Name the blood parasite species.
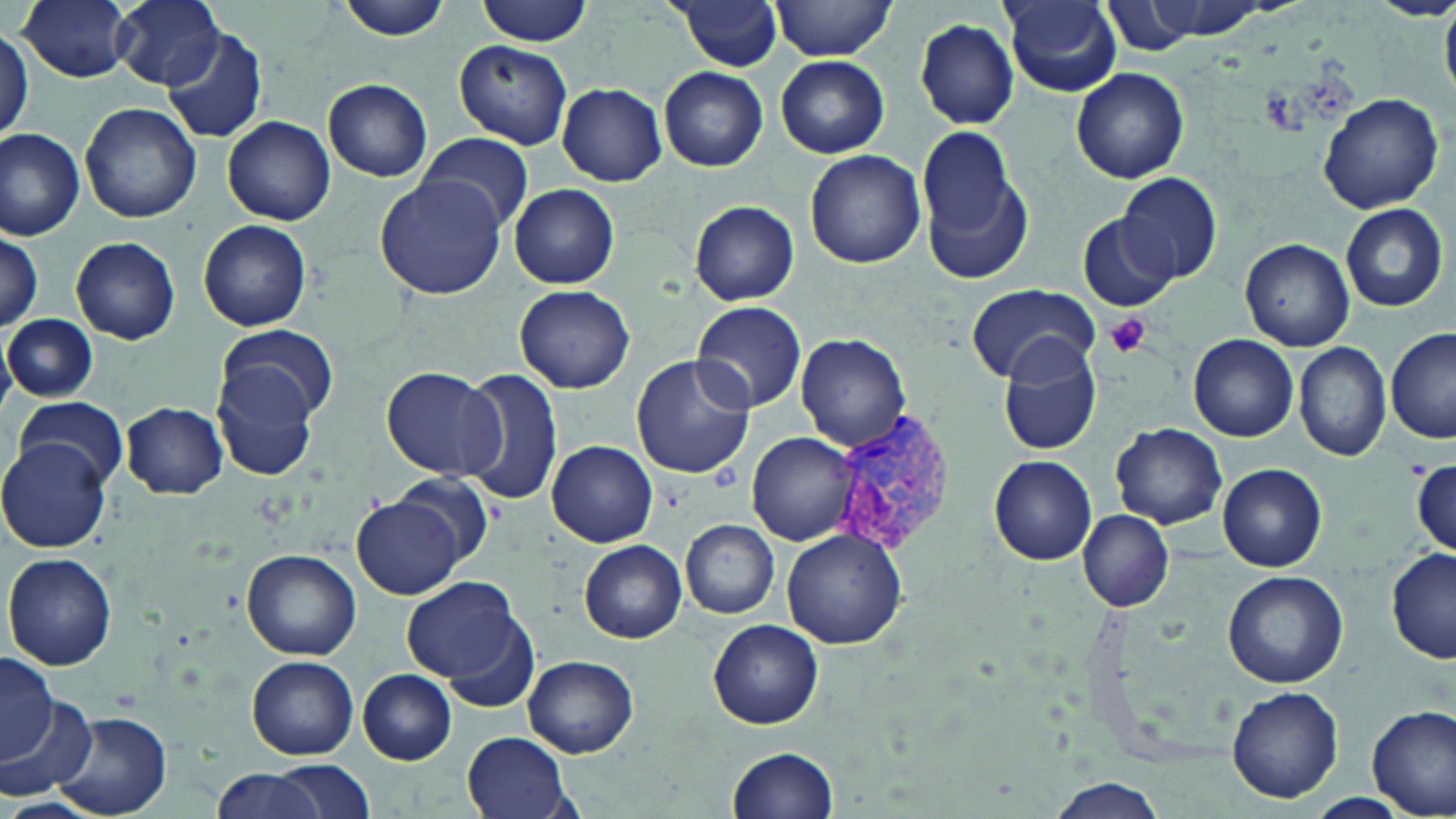

Plasmodium vivax.

Summary:
  - Coordinate format: approximate bounding boxes as named x1/y1/x2/y2 corners in pixels
  - Plasmodium vivax-infected red blood cell locations: (x1=822, y1=416, x2=953, y2=559)
  - Uninfected red blood cell locations: (x1=17, y1=0, x2=134, y2=83), (x1=114, y1=0, x2=225, y2=90), (x1=333, y1=0, x2=454, y2=41), (x1=477, y1=0, x2=593, y2=45), (x1=673, y1=0, x2=783, y2=72), (x1=768, y1=0, x2=902, y2=61), (x1=1100, y1=0, x2=1203, y2=55), (x1=1371, y1=0, x2=1456, y2=21), (x1=1001, y1=1, x2=1123, y2=97), (x1=915, y1=18, x2=1020, y2=129), (x1=0, y1=29, x2=32, y2=143), (x1=162, y1=29, x2=267, y2=142), (x1=453, y1=41, x2=573, y2=150), (x1=777, y1=56, x2=889, y2=158), (x1=1070, y1=66, x2=1189, y2=184), (x1=659, y1=67, x2=767, y2=172), (x1=323, y1=78, x2=433, y2=182), (x1=557, y1=83, x2=667, y2=185), (x1=1318, y1=93, x2=1443, y2=213), (x1=80, y1=102, x2=202, y2=222), (x1=222, y1=114, x2=335, y2=225), (x1=917, y1=125, x2=1028, y2=272), (x1=0, y1=126, x2=87, y2=239), (x1=417, y1=132, x2=534, y2=233), (x1=804, y1=149, x2=924, y2=269), (x1=1115, y1=171, x2=1224, y2=284), (x1=374, y1=176, x2=508, y2=299), (x1=509, y1=184, x2=620, y2=289), (x1=689, y1=201, x2=799, y2=305), (x1=1339, y1=203, x2=1448, y2=313), (x1=1077, y1=212, x2=1179, y2=310), (x1=198, y1=218, x2=311, y2=331), (x1=0, y1=230, x2=43, y2=334), (x1=69, y1=235, x2=181, y2=345), (x1=1240, y1=239, x2=1355, y2=350), (x1=514, y1=284, x2=634, y2=393), (x1=964, y1=284, x2=1099, y2=384), (x1=691, y1=300, x2=808, y2=414), (x1=3, y1=313, x2=96, y2=403), (x1=220, y1=326, x2=339, y2=426), (x1=1386, y1=327, x2=1456, y2=442), (x1=793, y1=332, x2=912, y2=451), (x1=1189, y1=334, x2=1299, y2=440), (x1=1294, y1=342, x2=1391, y2=462), (x1=996, y1=344, x2=1100, y2=456), (x1=630, y1=356, x2=756, y2=479), (x1=214, y1=366, x2=322, y2=483), (x1=382, y1=367, x2=505, y2=480), (x1=457, y1=368, x2=564, y2=508), (x1=15, y1=395, x2=132, y2=492), (x1=120, y1=402, x2=228, y2=498), (x1=1110, y1=422, x2=1228, y2=529), (x1=748, y1=432, x2=864, y2=545), (x1=0, y1=437, x2=112, y2=552), (x1=546, y1=440, x2=658, y2=547), (x1=989, y1=456, x2=1096, y2=565), (x1=1413, y1=458, x2=1454, y2=557), (x1=1217, y1=463, x2=1327, y2=571), (x1=394, y1=473, x2=494, y2=565), (x1=354, y1=496, x2=463, y2=598), (x1=1078, y1=510, x2=1174, y2=613), (x1=681, y1=518, x2=780, y2=619), (x1=780, y1=528, x2=909, y2=648), (x1=579, y1=540, x2=687, y2=643), (x1=1387, y1=547, x2=1456, y2=663), (x1=241, y1=550, x2=360, y2=658), (x1=2, y1=553, x2=117, y2=671), (x1=1222, y1=569, x2=1348, y2=687), (x1=403, y1=576, x2=526, y2=690), (x1=447, y1=616, x2=539, y2=715), (x1=707, y1=619, x2=823, y2=730), (x1=0, y1=651, x2=58, y2=768), (x1=521, y1=653, x2=638, y2=758), (x1=246, y1=655, x2=359, y2=759), (x1=357, y1=669, x2=457, y2=764), (x1=1225, y1=685, x2=1344, y2=804), (x1=1, y1=689, x2=95, y2=802), (x1=1368, y1=705, x2=1455, y2=817), (x1=51, y1=710, x2=172, y2=819), (x1=462, y1=731, x2=572, y2=819), (x1=726, y1=747, x2=839, y2=819), (x1=269, y1=759, x2=376, y2=817), (x1=210, y1=768, x2=324, y2=819), (x1=1045, y1=777, x2=1168, y2=819), (x1=1307, y1=793, x2=1407, y2=816)
  - Platelet locations: (x1=1103, y1=312, x2=1154, y2=358)
  - Magnification: 1000x
  - Preparation: thin blood smear
  - Stain: May-Grünwald-Giemsa
  - Modality: light microscopy
  - Image size: 1456×819 pixels
  - Field of view: one of a larger specimen